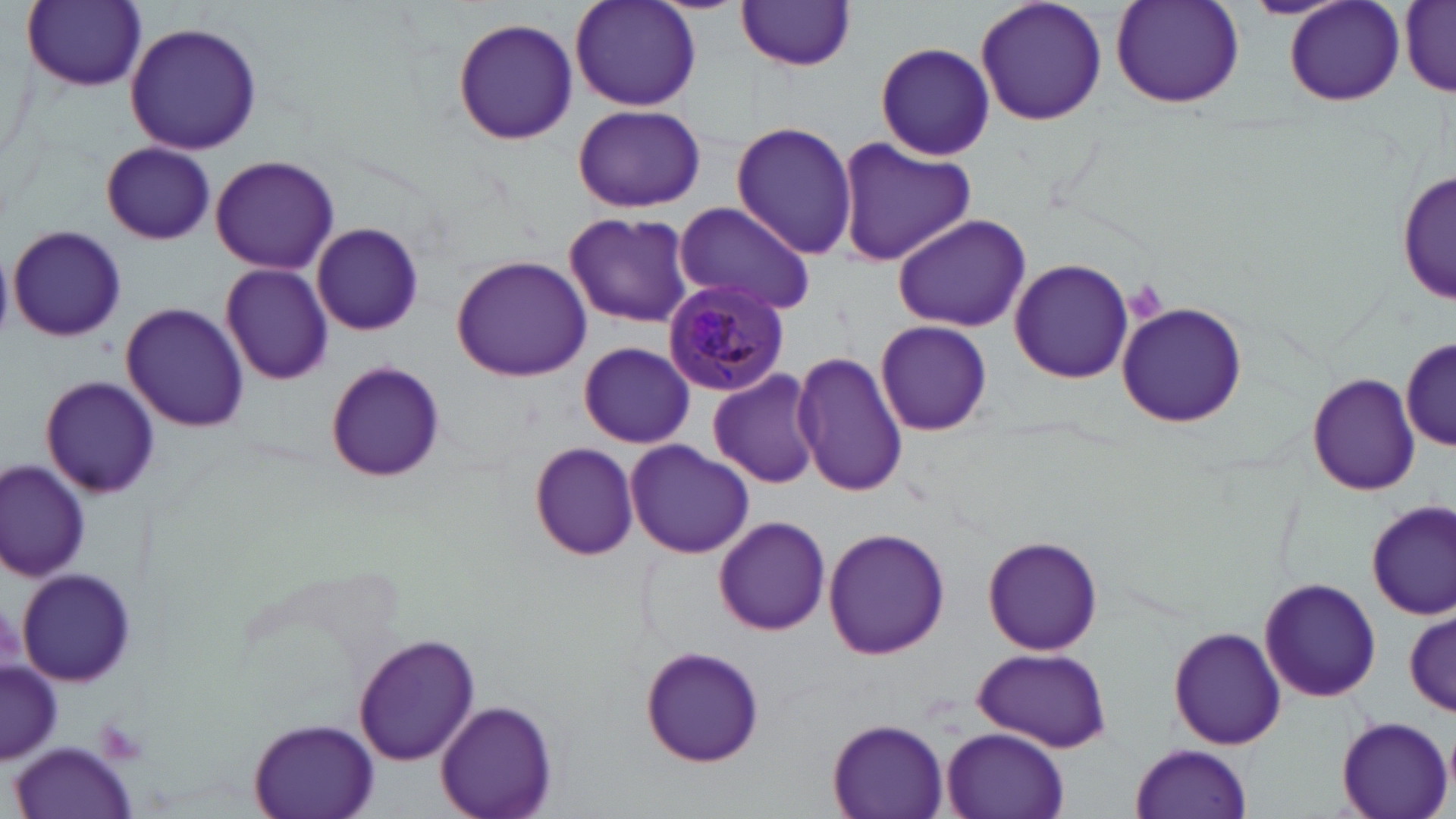

Approximate bounding boxes as named x1/y1/x2/y2 corners in pixels. Platelet locations: (x1=1123, y1=282, x2=1167, y2=319), (x1=95, y1=716, x2=150, y2=763). Plasmodium malariae-infected red blood cell locations: (x1=662, y1=282, x2=791, y2=397). Uninfected red blood cell locations: (x1=21, y1=0, x2=147, y2=91), (x1=569, y1=0, x2=702, y2=113), (x1=975, y1=0, x2=1107, y2=127), (x1=1109, y1=0, x2=1244, y2=107), (x1=1283, y1=0, x2=1404, y2=104), (x1=736, y1=1, x2=857, y2=71), (x1=1401, y1=4, x2=1456, y2=94), (x1=452, y1=17, x2=578, y2=145), (x1=123, y1=21, x2=263, y2=157), (x1=872, y1=41, x2=996, y2=161), (x1=572, y1=103, x2=705, y2=212), (x1=729, y1=120, x2=859, y2=256), (x1=835, y1=137, x2=977, y2=266), (x1=100, y1=142, x2=216, y2=244), (x1=210, y1=154, x2=340, y2=275), (x1=1399, y1=168, x2=1454, y2=306), (x1=671, y1=200, x2=818, y2=316), (x1=562, y1=211, x2=696, y2=328), (x1=890, y1=212, x2=1031, y2=332), (x1=312, y1=223, x2=425, y2=335), (x1=8, y1=224, x2=127, y2=343), (x1=0, y1=243, x2=17, y2=341), (x1=452, y1=255, x2=591, y2=381), (x1=1010, y1=259, x2=1135, y2=383), (x1=220, y1=262, x2=334, y2=386), (x1=1117, y1=302, x2=1247, y2=428), (x1=121, y1=303, x2=250, y2=433), (x1=875, y1=322, x2=993, y2=434), (x1=1402, y1=335, x2=1454, y2=454), (x1=579, y1=342, x2=694, y2=449), (x1=793, y1=351, x2=910, y2=496), (x1=325, y1=361, x2=443, y2=482), (x1=708, y1=368, x2=822, y2=489), (x1=1307, y1=373, x2=1420, y2=496), (x1=39, y1=375, x2=159, y2=500), (x1=627, y1=441, x2=754, y2=558), (x1=530, y1=442, x2=640, y2=561), (x1=0, y1=462, x2=89, y2=582), (x1=1366, y1=500, x2=1455, y2=618), (x1=713, y1=516, x2=831, y2=636), (x1=823, y1=527, x2=949, y2=659), (x1=983, y1=535, x2=1103, y2=656), (x1=18, y1=568, x2=138, y2=686), (x1=1260, y1=579, x2=1383, y2=702), (x1=1404, y1=610, x2=1456, y2=716), (x1=1169, y1=626, x2=1286, y2=751), (x1=354, y1=633, x2=479, y2=766), (x1=639, y1=643, x2=766, y2=768), (x1=971, y1=647, x2=1112, y2=752), (x1=2, y1=662, x2=59, y2=761), (x1=435, y1=699, x2=559, y2=819), (x1=1333, y1=715, x2=1452, y2=819), (x1=249, y1=716, x2=380, y2=819), (x1=827, y1=717, x2=950, y2=819), (x1=943, y1=727, x2=1069, y2=819), (x1=11, y1=742, x2=136, y2=819), (x1=1129, y1=743, x2=1254, y2=819). Slide-level diagnosis: Plasmodium malariae. May-Grünwald-Giemsa stain. Light microscopy. Image is 1456×819 pixels. 1000x magnification. Single field of view. Thin blood smear.